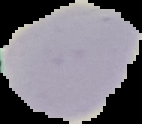 Malaria status: uninfected. From a thin blood smear. Image is 142×124 pixels. Cell region segmented out of the field of view; the surrounding area is masked to black.